Give the extent of all Plasmodium falciparum-infected red blood cells.
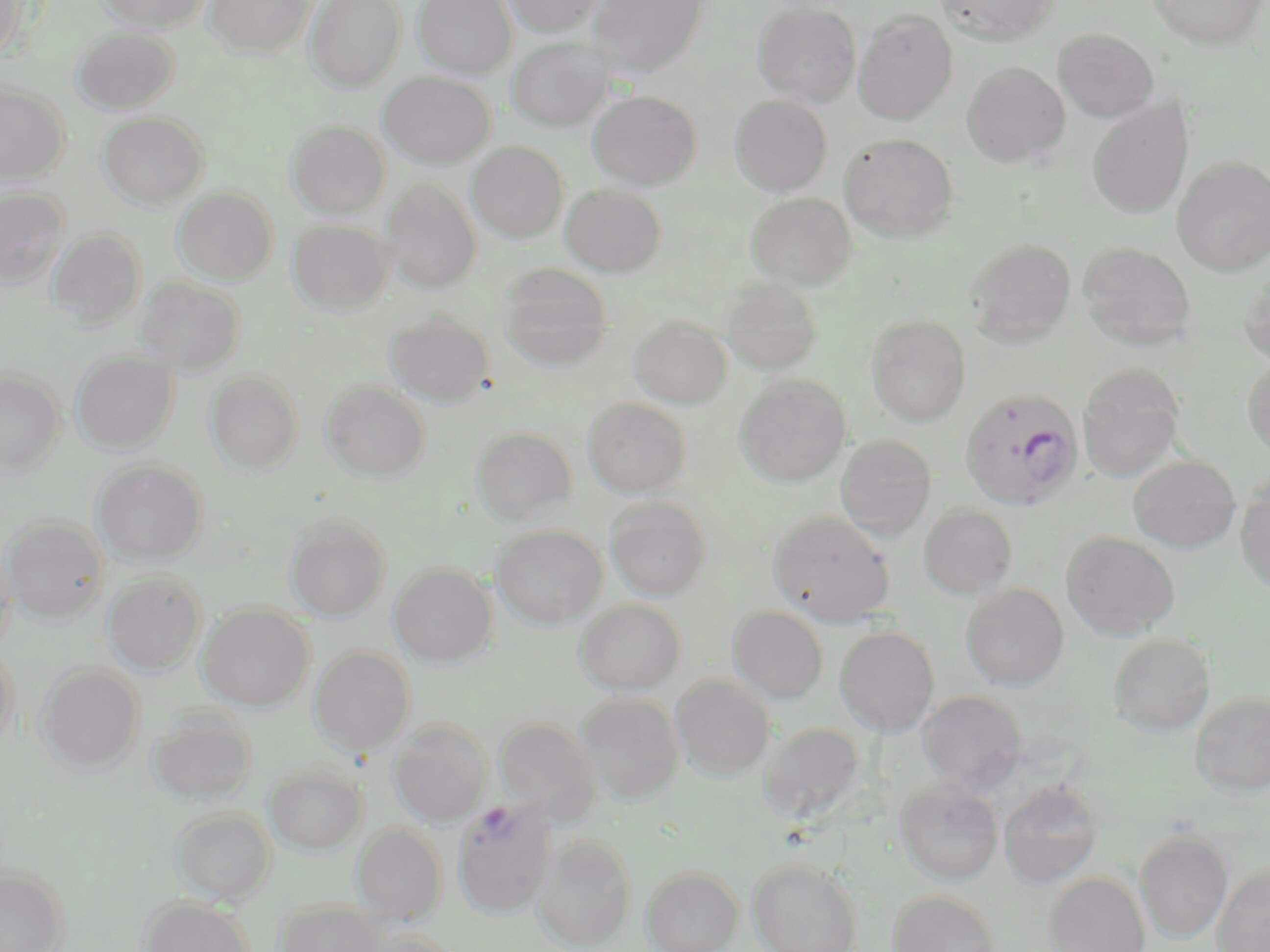

Approximate bounding boxes as [x1, y1, x2, y2] in pixels.
Plasmodium falciparum-infected red blood cells: [960, 387, 1084, 511], [452, 801, 558, 919].

Summary:
  - Uninfected red blood cell locations: [0, 0, 30, 61], [98, 0, 212, 31], [206, 0, 315, 59], [305, 0, 405, 91], [412, 0, 516, 79], [501, 0, 603, 37], [588, 0, 709, 78], [936, 0, 1060, 47], [1147, 0, 1268, 49], [752, 2, 861, 107], [854, 9, 957, 124], [72, 26, 179, 113], [1053, 29, 1159, 123], [507, 38, 611, 132], [962, 62, 1070, 168], [379, 73, 495, 168], [0, 83, 70, 184], [588, 90, 702, 190], [730, 95, 832, 196], [1088, 99, 1194, 219], [98, 112, 209, 209], [287, 120, 390, 219], [839, 133, 959, 242], [468, 142, 568, 243], [1173, 156, 1270, 277], [381, 180, 481, 293], [561, 184, 666, 277], [173, 186, 278, 285], [0, 187, 69, 287], [746, 192, 856, 290], [288, 218, 395, 316], [47, 227, 147, 330], [965, 238, 1076, 349], [1078, 242, 1196, 351], [499, 263, 613, 373], [1239, 270, 1270, 366], [134, 277, 246, 375], [722, 278, 823, 376], [384, 309, 494, 407], [866, 315, 970, 427], [629, 316, 732, 408], [72, 350, 178, 453], [1243, 354, 1270, 461], [1078, 362, 1185, 481], [0, 369, 64, 473], [206, 370, 304, 474], [735, 374, 851, 486], [321, 381, 430, 482], [582, 398, 691, 499], [471, 426, 577, 527], [835, 435, 937, 540], [1129, 455, 1241, 553], [94, 459, 208, 567], [1235, 474, 1270, 597], [605, 497, 712, 601], [919, 504, 1018, 600], [766, 509, 895, 627], [3, 514, 109, 624], [284, 514, 391, 621], [491, 524, 607, 630], [1062, 530, 1180, 641], [0, 532, 17, 655], [388, 562, 497, 666], [102, 570, 207, 674], [960, 583, 1069, 690], [574, 599, 685, 695], [198, 603, 314, 711], [726, 606, 828, 704], [836, 627, 939, 736], [1108, 634, 1216, 737], [0, 641, 19, 751], [309, 646, 415, 756], [36, 663, 145, 773], [671, 675, 774, 780], [917, 690, 1028, 790], [1190, 691, 1270, 797], [575, 694, 684, 804], [146, 708, 258, 806], [494, 717, 601, 824], [388, 718, 491, 826], [758, 722, 866, 824], [265, 764, 368, 855], [895, 779, 1004, 886], [997, 780, 1105, 889], [171, 807, 276, 905], [352, 823, 446, 923], [1134, 829, 1233, 944], [531, 834, 636, 951], [747, 858, 863, 952], [1211, 860, 1270, 952], [641, 865, 743, 952], [0, 866, 69, 952], [1044, 872, 1151, 952], [887, 889, 1001, 952], [141, 896, 256, 952], [276, 900, 385, 952]
  - Slide-level diagnosis: Plasmodium falciparum
  - Magnification: 1000x
  - Field of view: one of a larger specimen
  - Stain: May-Grünwald-Giemsa
  - Preparation: thin blood smear
  - Modality: optical microscopy
  - Image size: 1270×952 pixels